Identify the cell.
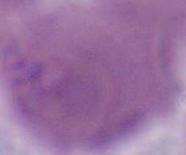
This is an erythrocyte.

Summary:
  - Modality: photomicrograph
  - Magnification: 1000x